Name the parasite shown.
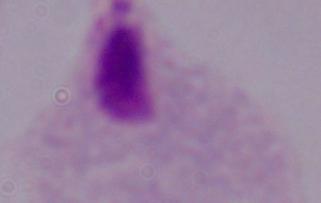

This is a trichomonad.

Photomicrograph. Captured at 1000x magnification.